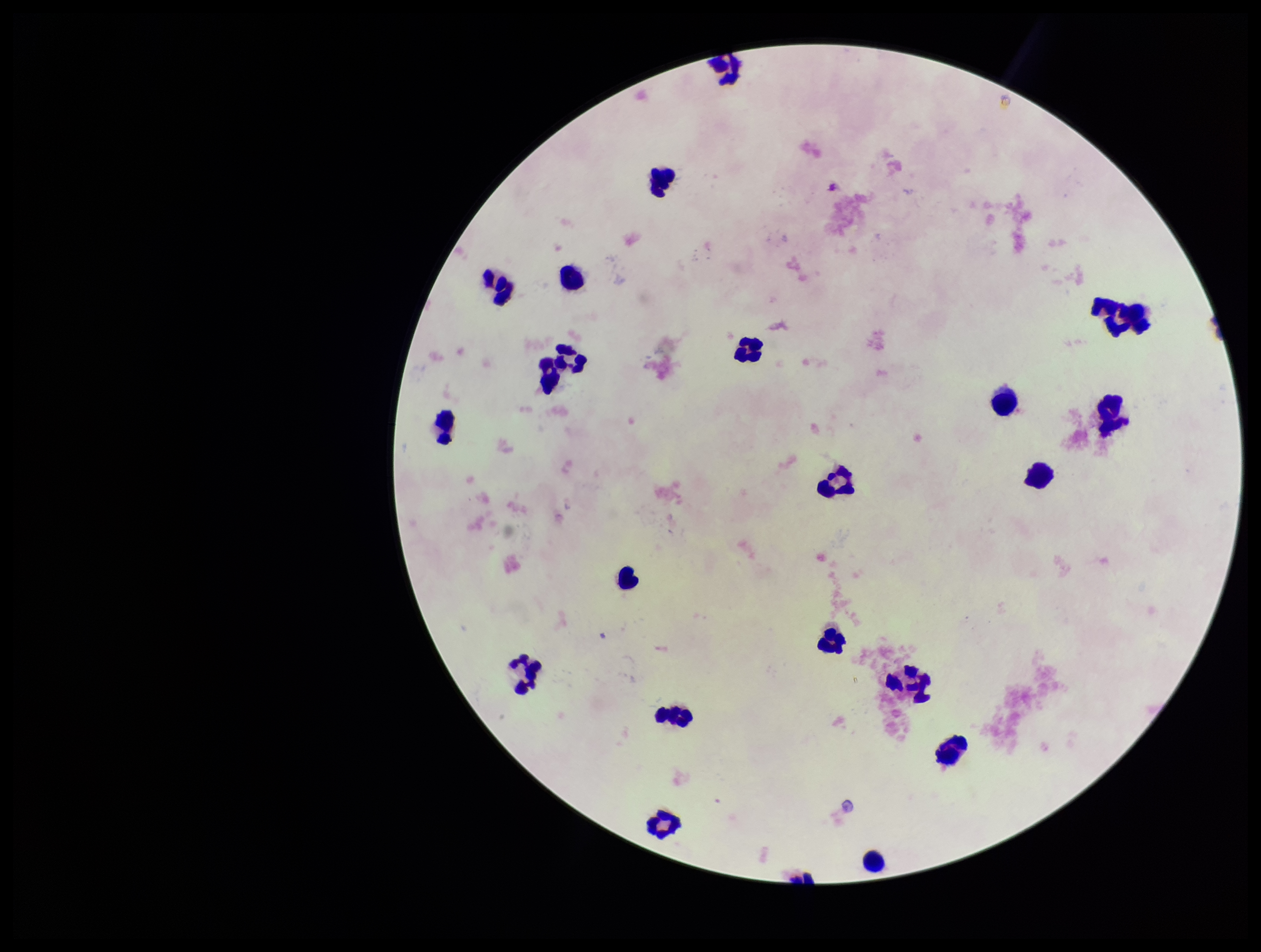
Patient malaria status: negative. Smartphone photograph taken through the eyepiece of a microscope. One field from this slide. Stained with Giemsa. Leukocyte count: 22. Image is 1261×952 pixels. Preparation: thick smear. Parasite count: 0. Plasmodium parasites: none seen.